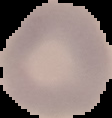

image size = 112×118 pixels
malaria status = uninfected
preparation = thin blood smear
image type = segmented cell region on a black background